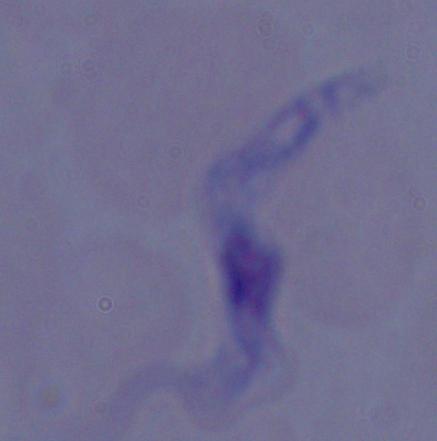

Captured at 1000x magnification. A trypanosome is seen. Photomicrograph.